Locate every blood parasite and identify its species.
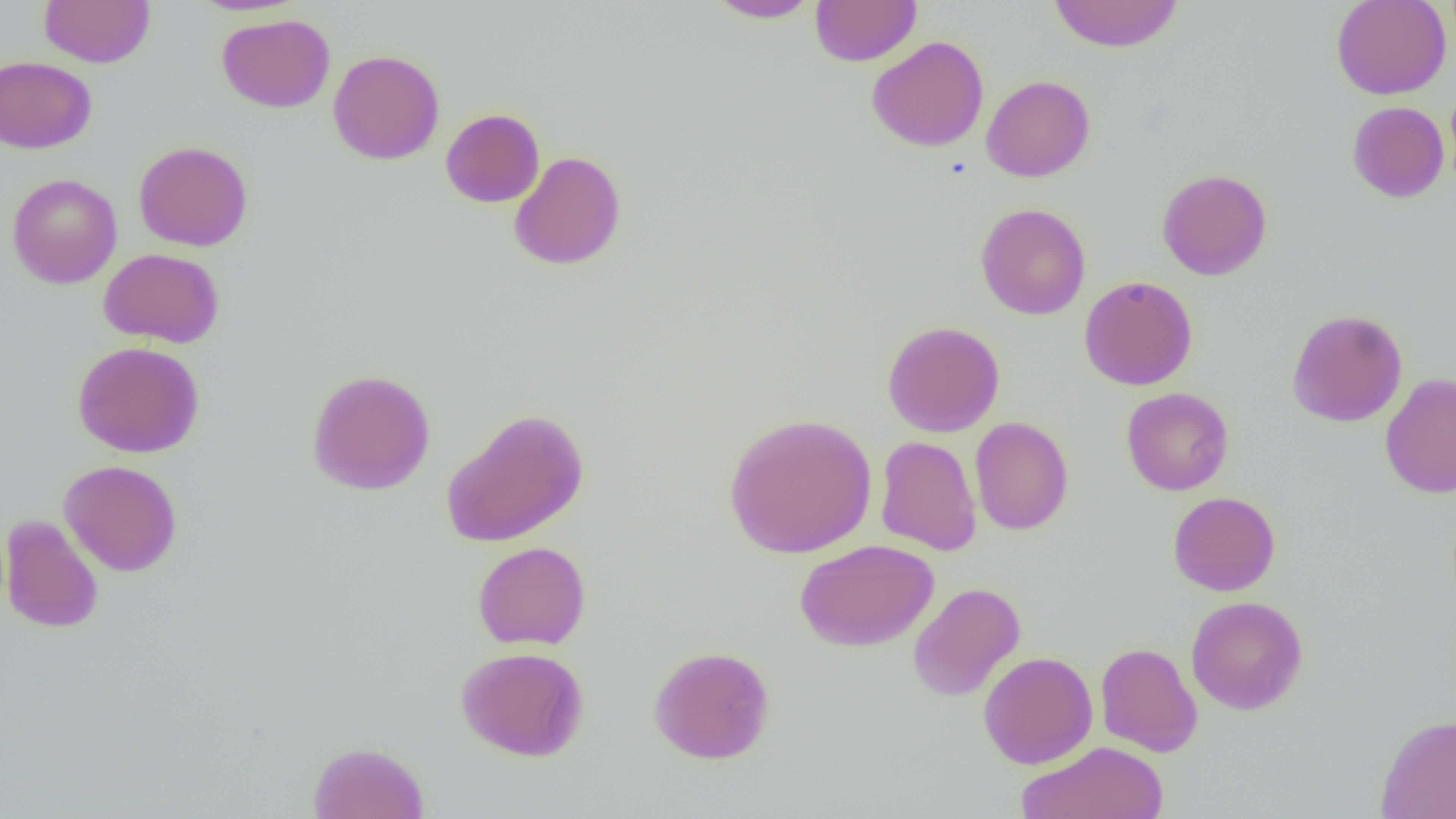

No blood parasites seen.

slide_level_diagnosis: negative for blood parasites
uninfected_red_blood_cell_locations: 'approximate bounding boxes as named x1/y1/x2/y2 corners in pixels: (x1=39, y1=0, x2=155, y2=67), (x1=706, y1=0, x2=821, y2=22), (x1=810, y1=0, x2=922, y2=66), (x1=1047, y1=0, x2=1184, y2=53), (x1=1331, y1=0, x2=1451, y2=100), (x1=217, y1=13, x2=335, y2=112), (x1=866, y1=35, x2=989, y2=152), (x1=327, y1=49, x2=445, y2=165), (x1=0, y1=56, x2=97, y2=153), (x1=981, y1=75, x2=1095, y2=182), (x1=1347, y1=101, x2=1449, y2=203), (x1=440, y1=109, x2=544, y2=207), (x1=133, y1=141, x2=253, y2=251), (x1=509, y1=151, x2=627, y2=271), (x1=1157, y1=168, x2=1273, y2=280), (x1=7, y1=173, x2=122, y2=288), (x1=975, y1=203, x2=1091, y2=320), (x1=99, y1=248, x2=224, y2=348), (x1=1079, y1=276, x2=1198, y2=390), (x1=1286, y1=308, x2=1407, y2=427), (x1=882, y1=320, x2=1004, y2=437), (x1=72, y1=341, x2=205, y2=458), (x1=306, y1=368, x2=436, y2=495), (x1=1380, y1=373, x2=1456, y2=499), (x1=1121, y1=387, x2=1234, y2=496), (x1=441, y1=407, x2=590, y2=547), (x1=722, y1=412, x2=877, y2=558), (x1=970, y1=416, x2=1074, y2=535), (x1=875, y1=435, x2=982, y2=556), (x1=59, y1=460, x2=183, y2=577), (x1=1167, y1=491, x2=1281, y2=596), (x1=1, y1=514, x2=104, y2=634), (x1=795, y1=539, x2=939, y2=651), (x1=472, y1=541, x2=591, y2=650), (x1=907, y1=582, x2=1025, y2=702), (x1=1186, y1=595, x2=1308, y2=715), (x1=1095, y1=642, x2=1203, y2=757), (x1=648, y1=645, x2=776, y2=764), (x1=455, y1=646, x2=589, y2=762), (x1=978, y1=651, x2=1098, y2=769), (x1=1375, y1=713, x2=1456, y2=818), (x1=307, y1=740, x2=430, y2=819), (x1=1016, y1=741, x2=1170, y2=818)'
field_of_view: one of a larger specimen
preparation: thin blood film
image_size: 1456×819 pixels
magnification: 1000x
modality: optical microscopy